Name the blood parasite species.
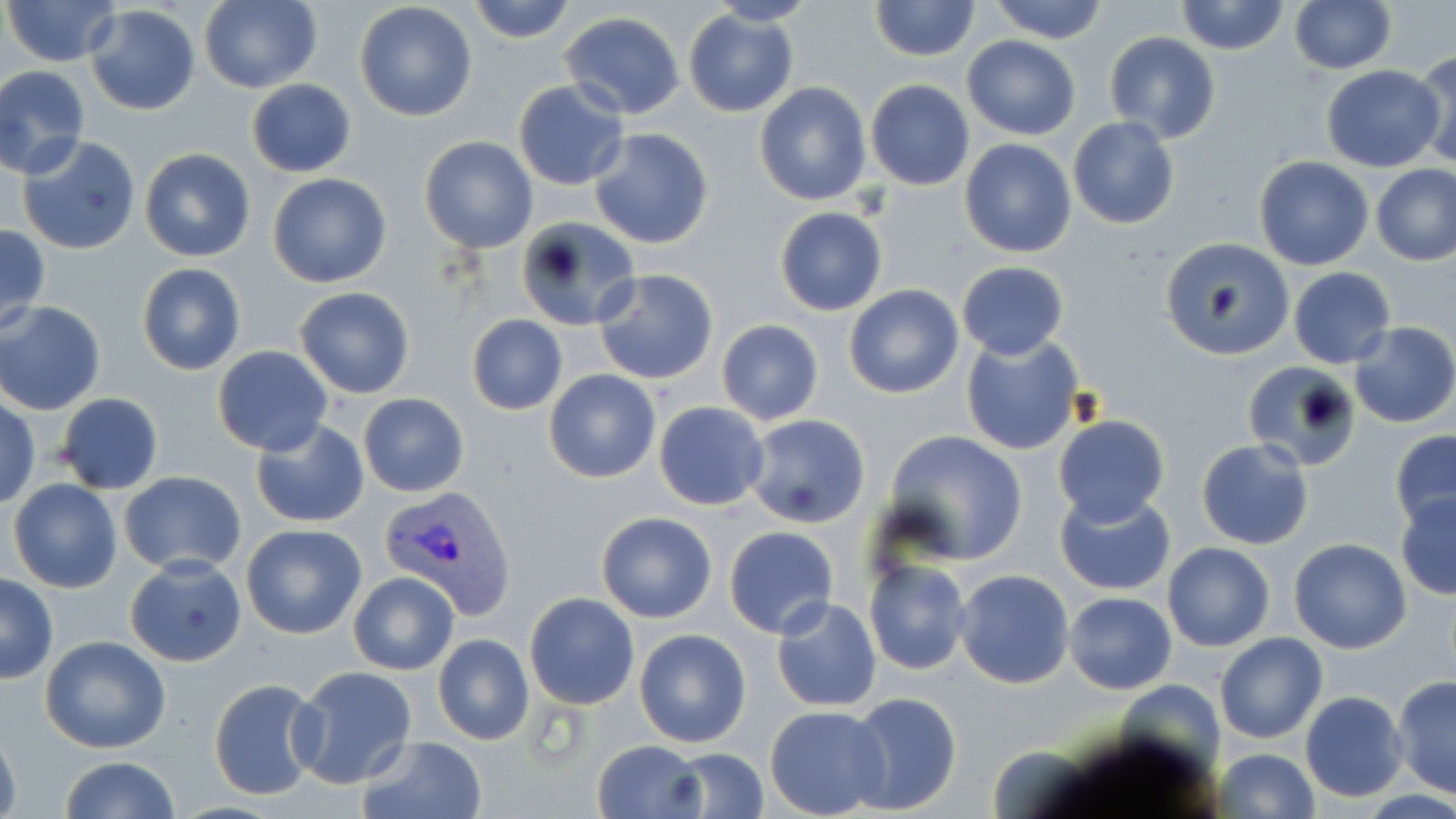
Plasmodium vivax.

Approximate bounding boxes as (x1, y1, x2, y2) in pixels. Uninfected red blood cell locations: (4, 0, 121, 67), (200, 0, 322, 94), (467, 0, 576, 44), (701, 0, 818, 26), (1287, 0, 1396, 74), (354, 1, 478, 123), (867, 1, 982, 61), (985, 1, 1112, 43), (1174, 1, 1289, 54), (83, 3, 201, 115), (682, 8, 798, 117), (560, 10, 686, 120), (1102, 33, 1221, 143), (961, 35, 1081, 140), (1412, 49, 1456, 171), (1320, 64, 1444, 172), (0, 65, 91, 179), (246, 78, 358, 177), (865, 80, 974, 190), (512, 81, 628, 190), (754, 81, 872, 206), (1067, 116, 1180, 230), (585, 127, 713, 250), (15, 135, 142, 256), (419, 135, 539, 254), (958, 138, 1078, 257), (139, 147, 256, 262), (1254, 156, 1374, 271), (1370, 163, 1455, 266), (267, 171, 392, 288), (774, 206, 888, 316), (513, 212, 641, 331), (0, 224, 50, 336), (1158, 237, 1288, 359), (956, 260, 1069, 359), (136, 263, 246, 376), (1288, 266, 1397, 368), (592, 268, 718, 386), (844, 284, 964, 399), (294, 285, 416, 399), (1, 301, 106, 415), (466, 314, 567, 415), (716, 319, 824, 425), (1348, 321, 1456, 429), (959, 332, 1084, 456), (212, 346, 334, 456), (1242, 360, 1365, 472), (544, 368, 661, 484), (56, 391, 165, 495), (358, 394, 469, 496), (0, 398, 40, 509), (654, 402, 769, 511), (743, 413, 872, 529), (1052, 414, 1169, 525), (250, 418, 371, 529), (884, 428, 1029, 563), (1389, 431, 1456, 533), (1196, 439, 1316, 550), (119, 471, 248, 576), (9, 478, 123, 593), (1054, 487, 1178, 596), (1394, 494, 1456, 599), (596, 512, 718, 623), (240, 524, 365, 639), (723, 526, 840, 639), (1288, 538, 1412, 654), (1162, 541, 1275, 651), (124, 557, 247, 668), (863, 559, 972, 675), (953, 569, 1075, 690), (349, 571, 459, 676), (0, 572, 58, 684), (523, 592, 639, 709), (1063, 592, 1178, 694), (770, 596, 883, 712), (634, 628, 752, 748), (1214, 632, 1327, 744), (433, 634, 534, 745), (39, 636, 170, 754), (289, 666, 419, 790), (1392, 674, 1456, 799), (208, 677, 324, 800), (844, 690, 963, 814), (1300, 691, 1408, 802), (764, 705, 891, 817), (0, 723, 21, 819), (357, 735, 487, 819), (592, 739, 706, 819), (662, 748, 769, 818), (1213, 748, 1319, 819), (59, 756, 182, 818). Plasmodium vivax-infected red blood cell locations: (380, 485, 515, 615). Light microscopy. Thin blood film. Single field of view. 1000x magnification. Image is 1456×819 pixels. May-Grünwald-Giemsa-stained preparation.